Assess this cell for malaria.
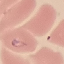
Parasitized.

Summary:
  - Capture: smartphone camera at the microscope eyepiece
  - Stain: Giemsa
  - Image type: cell patch, automatically extracted from a larger field of view and resized to 64 × 64 pixels
  - Preparation: thin blood film